Locate every Plasmodium falciparum-infected red blood cell.
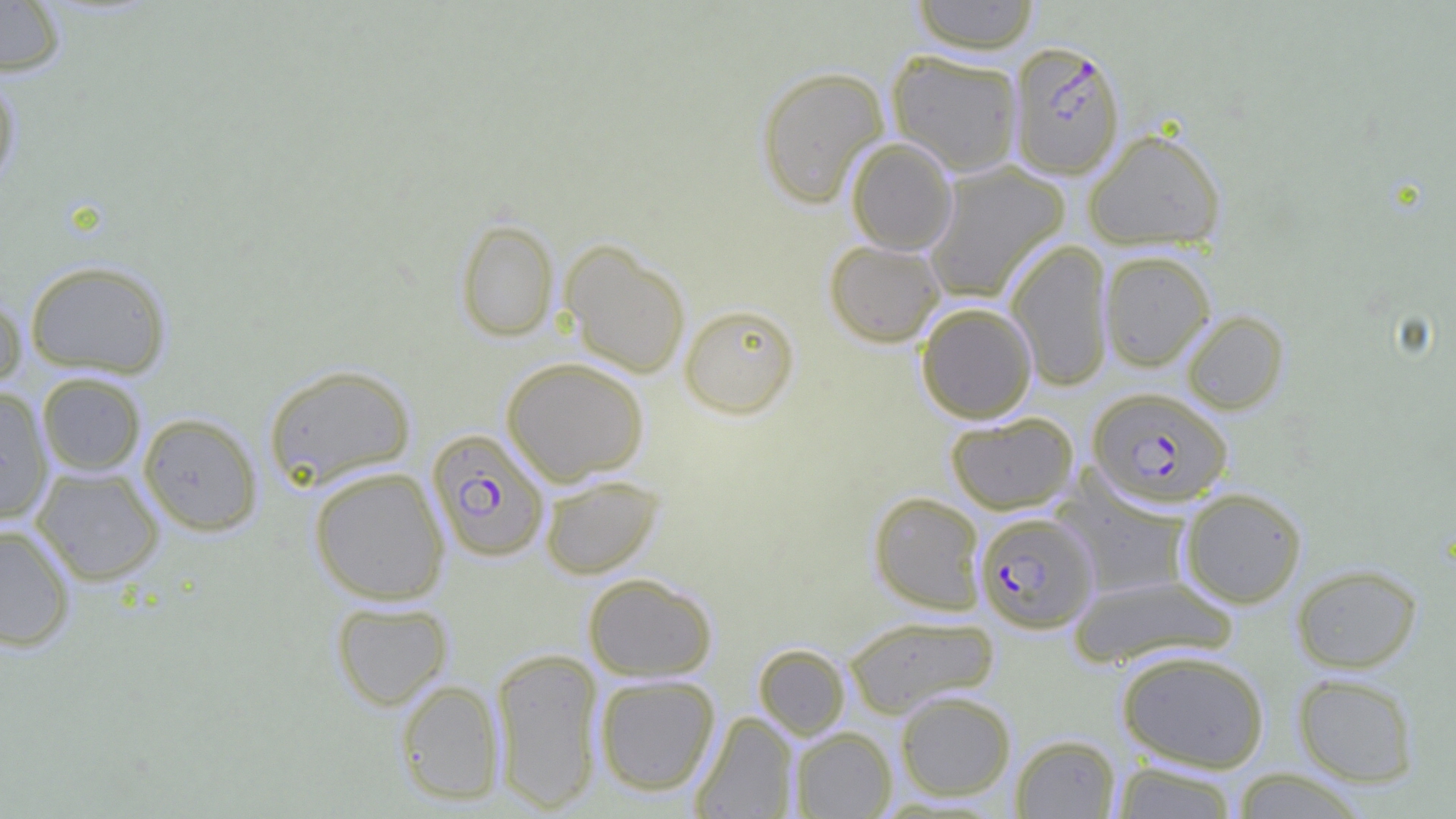

Approximate bounding boxes as (x1,y1)-(x2,y2) corner pairs in pixels.
Plasmodium falciparum-infected red blood cells: (1008,40)-(1125,180), (1089,388)-(1233,508), (427,428)-(550,562), (975,512)-(1099,633).

Uninfected red blood cell locations: (910,0)-(1040,54), (0,1)-(66,76), (887,49)-(1024,176), (755,66)-(889,208), (0,73)-(22,195), (1083,128)-(1226,251), (846,137)-(958,255), (922,161)-(1069,303), (456,218)-(559,342), (824,239)-(946,347), (1005,239)-(1114,391), (559,240)-(691,378), (1100,250)-(1215,371), (24,259)-(172,378), (0,288)-(27,393), (916,302)-(1037,423), (679,303)-(800,419), (1181,310)-(1289,414), (501,357)-(650,485), (263,363)-(416,490), (37,372)-(146,476), (0,386)-(54,523), (138,412)-(263,536), (945,412)-(1078,515), (31,465)-(164,585), (309,466)-(449,605), (540,474)-(663,579), (1058,475)-(1193,600), (1179,487)-(1307,608), (868,491)-(986,615), (0,523)-(77,652), (1291,563)-(1422,673), (583,573)-(718,681), (1067,574)-(1237,668), (330,600)-(453,710), (843,614)-(999,718), (753,643)-(851,740), (490,647)-(605,813), (1116,649)-(1270,772), (1293,673)-(1419,787), (594,674)-(720,795), (395,679)-(505,805), (895,690)-(1016,801), (691,711)-(798,818), (790,727)-(896,818), (1011,734)-(1121,818), (1108,761)-(1241,818), (1228,769)-(1371,818). Slide-level diagnosis: Plasmodium falciparum. One field of a larger specimen. Image is 1456×819 pixels. Captured at 1000x magnification. Optical microscopy. Thin blood film.